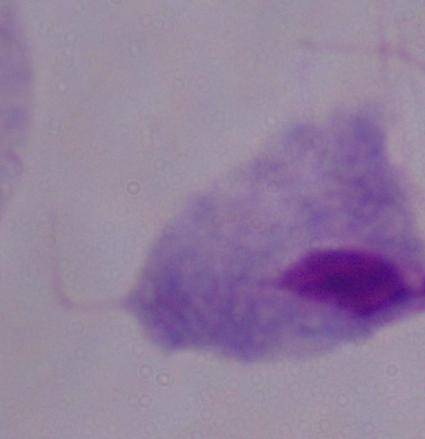

identification: trichomonad
magnification: 1000x
modality: photomicrograph